State which parasite is depicted.
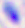
Toxoplasma gondii.

magnification = 400x
modality = photomicrograph